Classify this cell by malaria status.
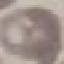

It is uninfected.

Summary:
  - Capture: smartphone through the microscope eyepiece
  - Stain: Giemsa
  - Image type: automatically extracted cell patch, resized to 64 × 64 pixels
  - Preparation: thin blood film